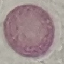

Malaria status: uninfected. Photographed with a smartphone camera at the microscope eyepiece. Cell patch, automatically extracted from a larger field of view and resized to 64 × 64 pixels. Giemsa-stained preparation. Thin blood film.